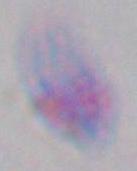
Summary:
  - Identification: Toxoplasma gondii
  - Modality: micrograph
  - Magnification: 1000x